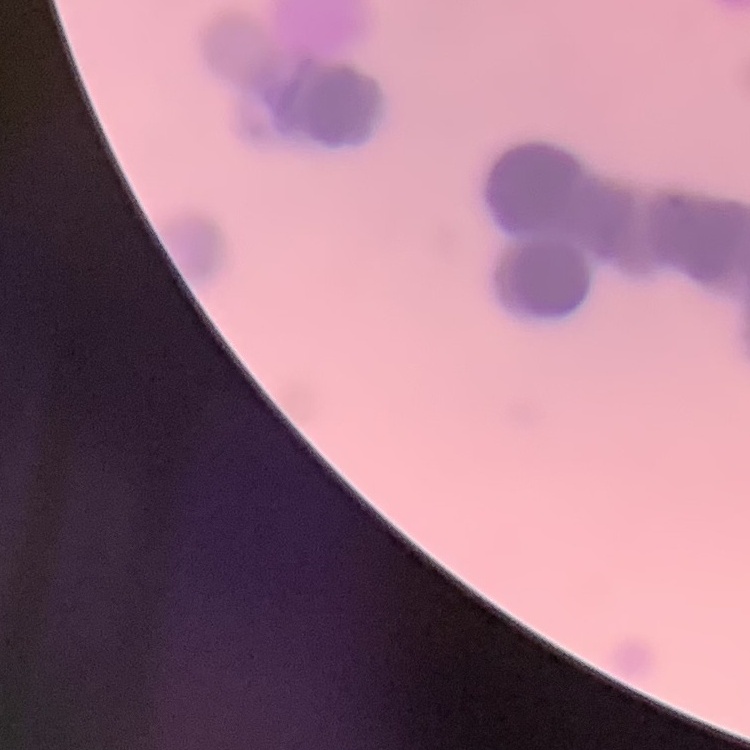
The red blood cells exhibit rouleaux formation. Thin blood smear. Field's or Giemsa stain. Square crop of a larger photomicrograph.